Assess this cell for malaria.
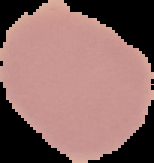

It is uninfected.

Summary:
  - Preparation: thin blood film
  - Image type: segmented cell region with the area outside set to black
  - Image size: 154×163 pixels